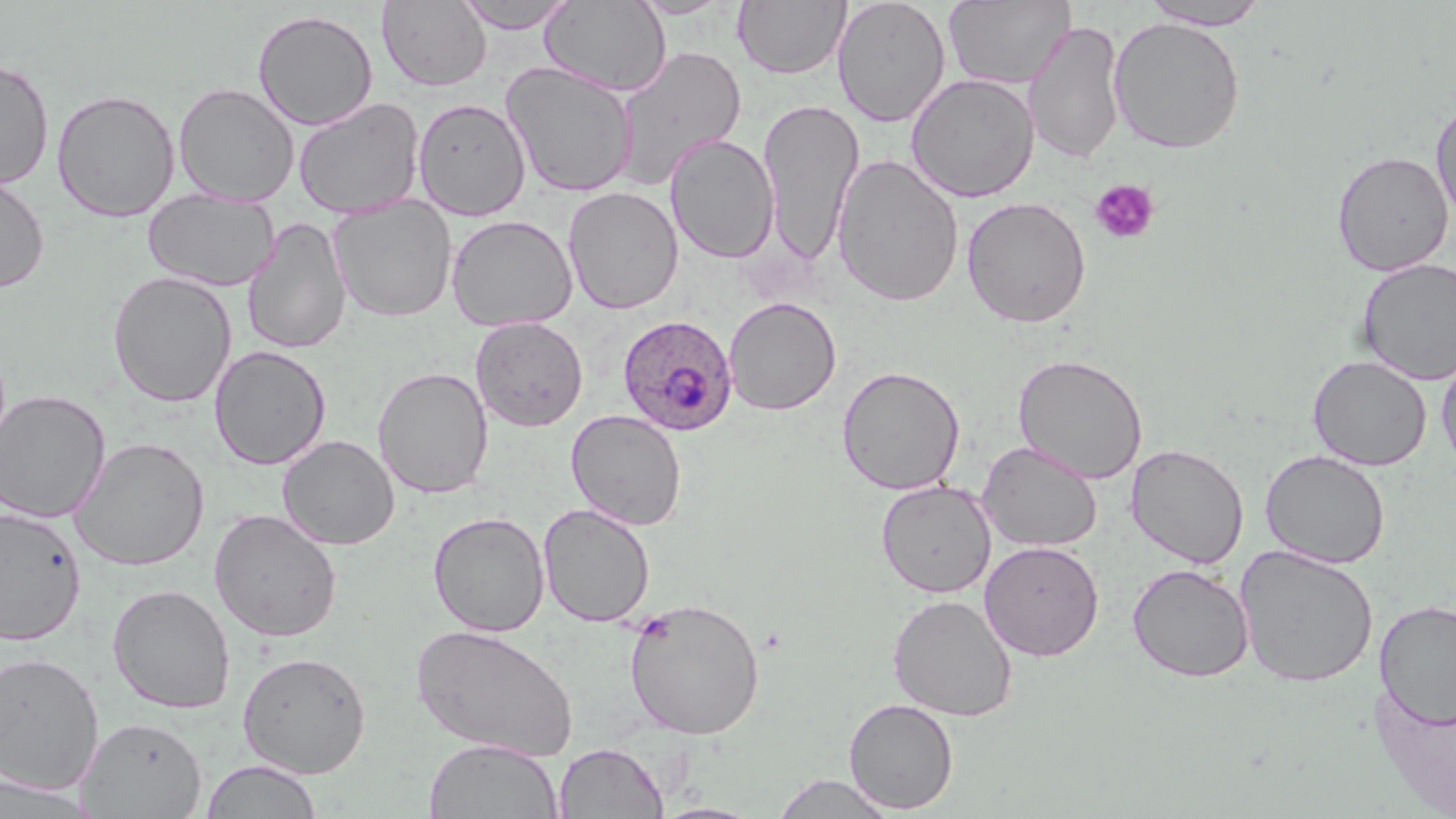

Summary:
  - Coordinate format: approximate bounding boxes as named x1/y1/x2/y2 corners in pixels
  - Platelet locations: (x1=1090, y1=178, x2=1160, y2=245)
  - Plasmodium ovale-infected red blood cell locations: (x1=618, y1=315, x2=738, y2=436)
  - Uninfected red blood cell locations: (x1=453, y1=0, x2=579, y2=33), (x1=540, y1=0, x2=671, y2=96), (x1=628, y1=0, x2=734, y2=19), (x1=733, y1=0, x2=849, y2=80), (x1=832, y1=0, x2=951, y2=128), (x1=377, y1=1, x2=492, y2=91), (x1=944, y1=1, x2=1075, y2=90), (x1=1140, y1=1, x2=1270, y2=30), (x1=252, y1=9, x2=379, y2=130), (x1=1109, y1=16, x2=1246, y2=154), (x1=1024, y1=19, x2=1126, y2=164), (x1=613, y1=46, x2=747, y2=189), (x1=0, y1=57, x2=55, y2=189), (x1=500, y1=61, x2=639, y2=197), (x1=906, y1=73, x2=1040, y2=203), (x1=173, y1=81, x2=299, y2=206), (x1=51, y1=88, x2=181, y2=222), (x1=1430, y1=96, x2=1456, y2=226), (x1=293, y1=97, x2=426, y2=218), (x1=412, y1=97, x2=532, y2=220), (x1=757, y1=99, x2=864, y2=265), (x1=665, y1=133, x2=780, y2=264), (x1=1332, y1=150, x2=1454, y2=276), (x1=831, y1=154, x2=965, y2=307), (x1=0, y1=172, x2=50, y2=294), (x1=563, y1=186, x2=684, y2=315), (x1=143, y1=190, x2=279, y2=291), (x1=328, y1=196, x2=457, y2=323), (x1=961, y1=196, x2=1091, y2=328), (x1=446, y1=214, x2=578, y2=332), (x1=243, y1=217, x2=352, y2=355), (x1=1356, y1=258, x2=1456, y2=385), (x1=108, y1=270, x2=237, y2=408), (x1=723, y1=296, x2=841, y2=415), (x1=470, y1=316, x2=588, y2=431), (x1=209, y1=345, x2=331, y2=470), (x1=1436, y1=346, x2=1456, y2=473), (x1=1013, y1=353, x2=1148, y2=484), (x1=1308, y1=355, x2=1432, y2=471), (x1=836, y1=365, x2=966, y2=495), (x1=372, y1=366, x2=493, y2=499), (x1=0, y1=390, x2=111, y2=522), (x1=565, y1=409, x2=688, y2=530), (x1=278, y1=434, x2=400, y2=550), (x1=70, y1=436, x2=209, y2=571), (x1=977, y1=441, x2=1103, y2=552), (x1=1127, y1=443, x2=1249, y2=569), (x1=1260, y1=449, x2=1390, y2=569), (x1=876, y1=480, x2=997, y2=598), (x1=538, y1=503, x2=655, y2=628), (x1=0, y1=506, x2=87, y2=647), (x1=208, y1=508, x2=343, y2=643), (x1=428, y1=511, x2=550, y2=636), (x1=979, y1=540, x2=1104, y2=661), (x1=1234, y1=544, x2=1379, y2=689), (x1=1127, y1=562, x2=1255, y2=682), (x1=107, y1=583, x2=235, y2=714), (x1=888, y1=593, x2=1018, y2=722), (x1=623, y1=596, x2=766, y2=740), (x1=1375, y1=599, x2=1456, y2=729), (x1=411, y1=623, x2=579, y2=761), (x1=237, y1=650, x2=371, y2=778), (x1=0, y1=651, x2=104, y2=795), (x1=1370, y1=672, x2=1456, y2=814), (x1=844, y1=698, x2=959, y2=814), (x1=77, y1=716, x2=207, y2=819), (x1=423, y1=738, x2=564, y2=819), (x1=555, y1=742, x2=668, y2=818), (x1=200, y1=759, x2=323, y2=818), (x1=770, y1=773, x2=896, y2=818), (x1=0, y1=775, x2=101, y2=816), (x1=653, y1=802, x2=763, y2=819)
  - Slide-level diagnosis: Plasmodium ovale
  - Preparation: thin blood smear
  - Magnification: 1000x
  - Image size: 1456×819 pixels
  - Field of view: one of a larger specimen
  - Stain: May-Grünwald-Giemsa
  - Modality: optical microscopy